Classify this cell by malaria status.
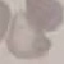
Uninfected.

image type = automatically extracted cell patch, resized to 64 × 64 pixels
capture = smartphone through the microscope eyepiece
stain = Giemsa
preparation = thin smear